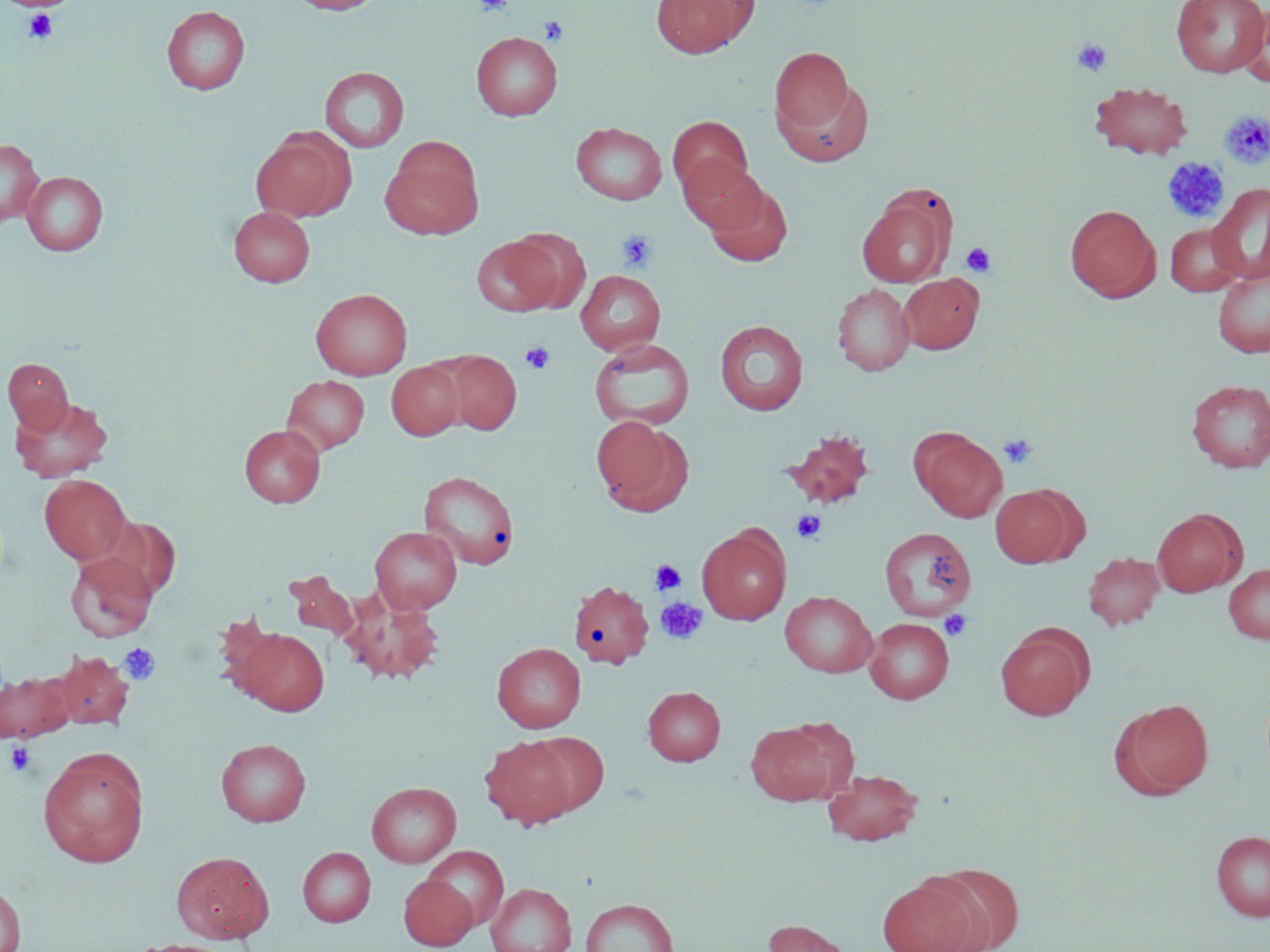

{
  "slide_level_diagnosis": "negative for blood parasites",
  "preparation": "thin blood film",
  "uninfected_red_blood_cell_locations": "approximate bounding boxes as (x1,y1)-(x2,y2) corner pairs in pixels: (287,0)-(384,14), (651,0)-(758,58), (1171,0)-(1269,77), (162,5)-(250,94), (1236,5)-(1270,88), (471,31)-(563,120), (769,46)-(857,143), (320,67)-(409,152), (1090,81)-(1192,160), (668,115)-(753,200), (570,122)-(667,205), (251,130)-(353,222), (0,138)-(44,226), (380,138)-(485,239), (678,156)-(767,234), (23,171)-(108,255), (704,180)-(793,267), (1208,184)-(1270,284), (858,185)-(960,286), (1065,203)-(1161,302), (229,206)-(315,287), (1165,223)-(1245,297), (506,227)-(591,313), (471,235)-(562,316), (575,269)-(666,355), (1213,269)-(1270,358), (898,273)-(983,354), (832,283)-(914,376), (311,288)-(412,380), (715,319)-(808,415), (588,338)-(696,431), (433,349)-(521,434), (3,358)-(73,433), (386,361)-(464,440), (282,375)-(369,455), (1186,379)-(1270,473), (10,395)-(114,482), (591,416)-(692,515), (239,424)-(325,507), (783,429)-(875,509), (914,431)-(1006,522), (418,470)-(520,570), (39,475)-(131,564), (990,484)-(1082,567), (1152,508)-(1247,597), (697,524)-(791,625), (370,526)-(462,614), (879,526)-(976,620), (65,552)-(158,641), (1083,552)-(1164,630), (1223,563)-(1270,643), (285,571)-(359,639), (569,580)-(654,668), (780,590)-(877,677), (343,592)-(444,684), (864,617)-(954,704), (995,626)-(1092,720), (234,627)-(329,715), (492,642)-(586,733), (50,650)-(134,729), (0,671)-(72,743), (643,686)-(725,765), (1115,698)-(1214,797), (746,719)-(847,805), (527,731)-(610,814), (480,735)-(577,829), (216,738)-(311,827), (39,747)-(149,868), (824,768)-(922,846), (367,781)-(461,867), (1211,830)-(1270,921), (423,845)-(508,930), (298,847)-(376,926), (171,851)-(274,943), (923,863)-(1025,952), (399,874)-(477,950), (877,877)-(981,952), (0,883)-(26,952), (486,883)-(577,952), (581,898)-(678,951), (762,918)-(853,952), (125,939)-(238,952)",
  "modality": "light microscopy",
  "field_of_view": "single",
  "image_size": "1270×952 pixels",
  "platelet_locations": "approximate bounding boxes as (x1,y1)-(x2,y2) corner pairs in pixels: (474,0)-(514,16), (23,10)-(59,45), (539,17)-(568,45), (1072,39)-(1112,77), (1219,110)-(1270,169), (1162,157)-(1229,223), (616,230)-(657,270), (961,242)-(997,278), (520,342)-(555,374), (999,433)-(1037,468), (792,510)-(826,544), (650,559)-(685,595), (656,597)-(707,644), (939,610)-(971,641), (119,643)-(160,686), (5,741)-(37,776)",
  "magnification": "1000x",
  "stain": "May-Grünwald-Giemsa"
}